Assess the morphology of the red blood cells.
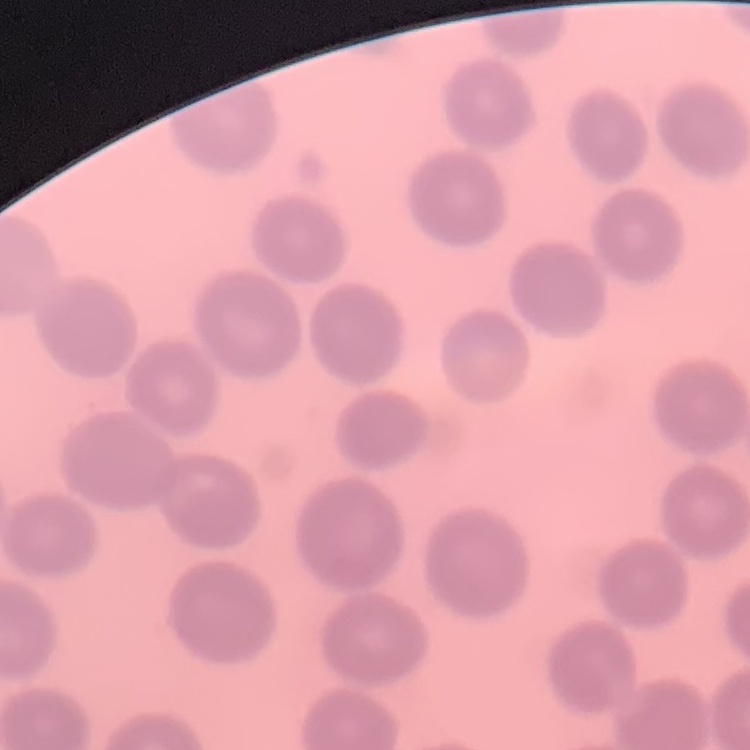
They show no rouleaux formation.

Thin blood smear. Stained with either Field's or Giemsa. Square crop of a larger photomicrograph.